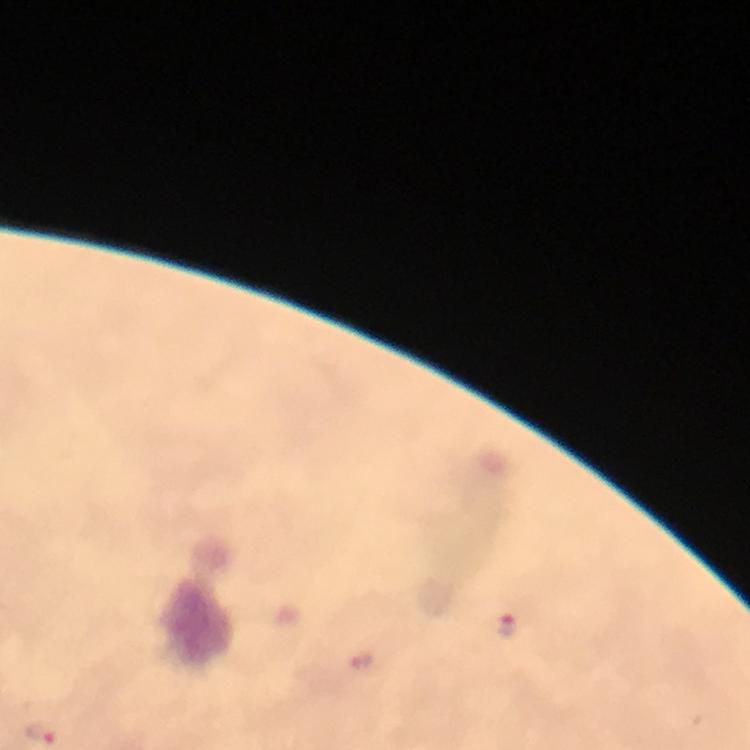

immersion oil = used
capture = smartphone photograph through a microscope
image size = 750×750 pixels
magnification = 100x
context = from a diagnostic examination for malaria
preparation = thick blood film
cropped from = a single field of view
stain = Giemsa
Plasmodium parasite locations = approximate object centers, in pixels from the top-left corner: (x=507, y=626), (x=361, y=660), (x=41, y=733)